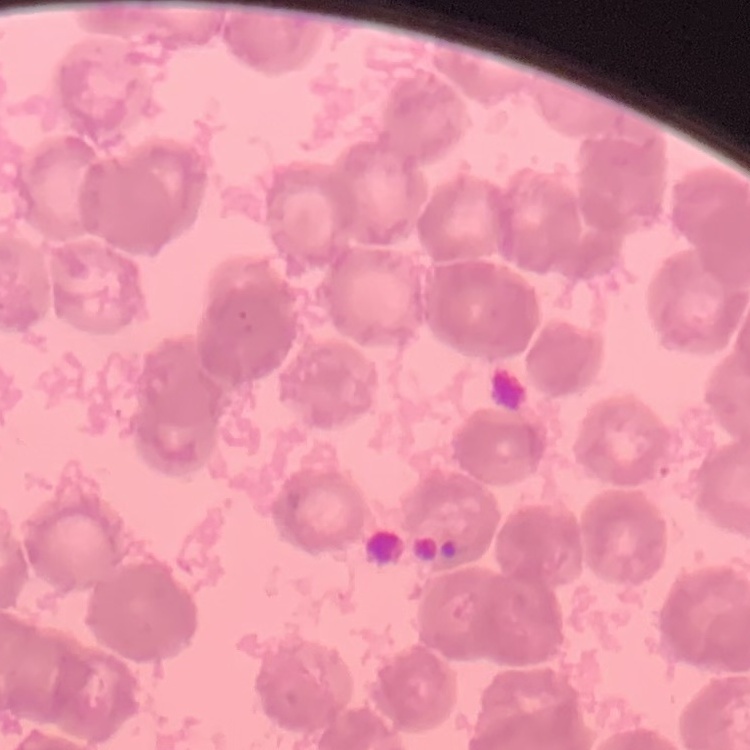
The red blood cells exhibit rouleaux formation. Stained with either Field's or Giemsa. One tile cut from a larger photomicrograph. Thin blood film.